State which cell type is depicted.
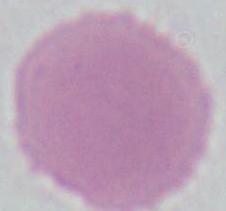
This is an erythrocyte.

1000x magnification. Micrograph.